Comment on the morphology of the red blood cells.
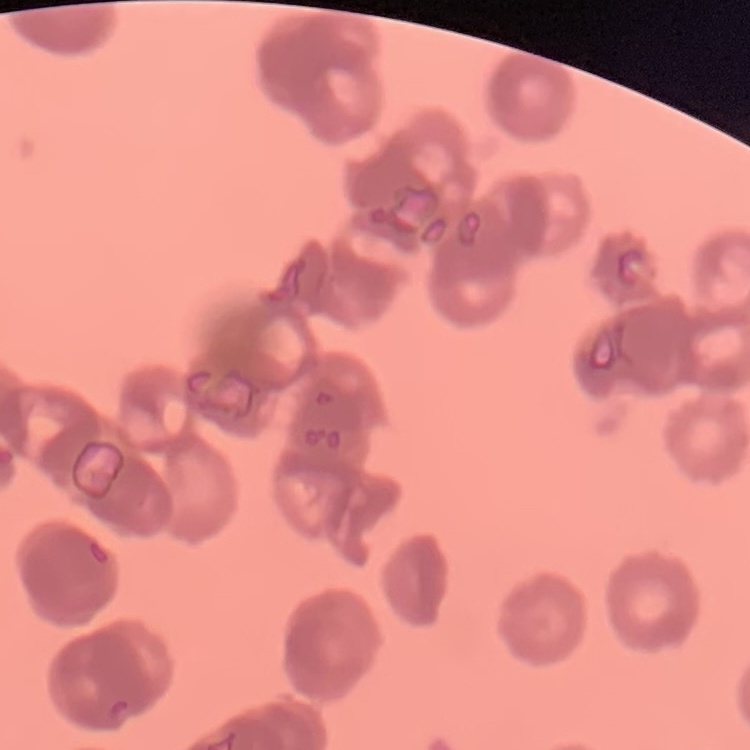

They show rouleaux formation.

Summary:
  - Preparation: thin blood smear
  - Image type: one tile cut from a larger photomicrograph
  - Stain: Field's or Giemsa